Locate and identify every blood parasite.
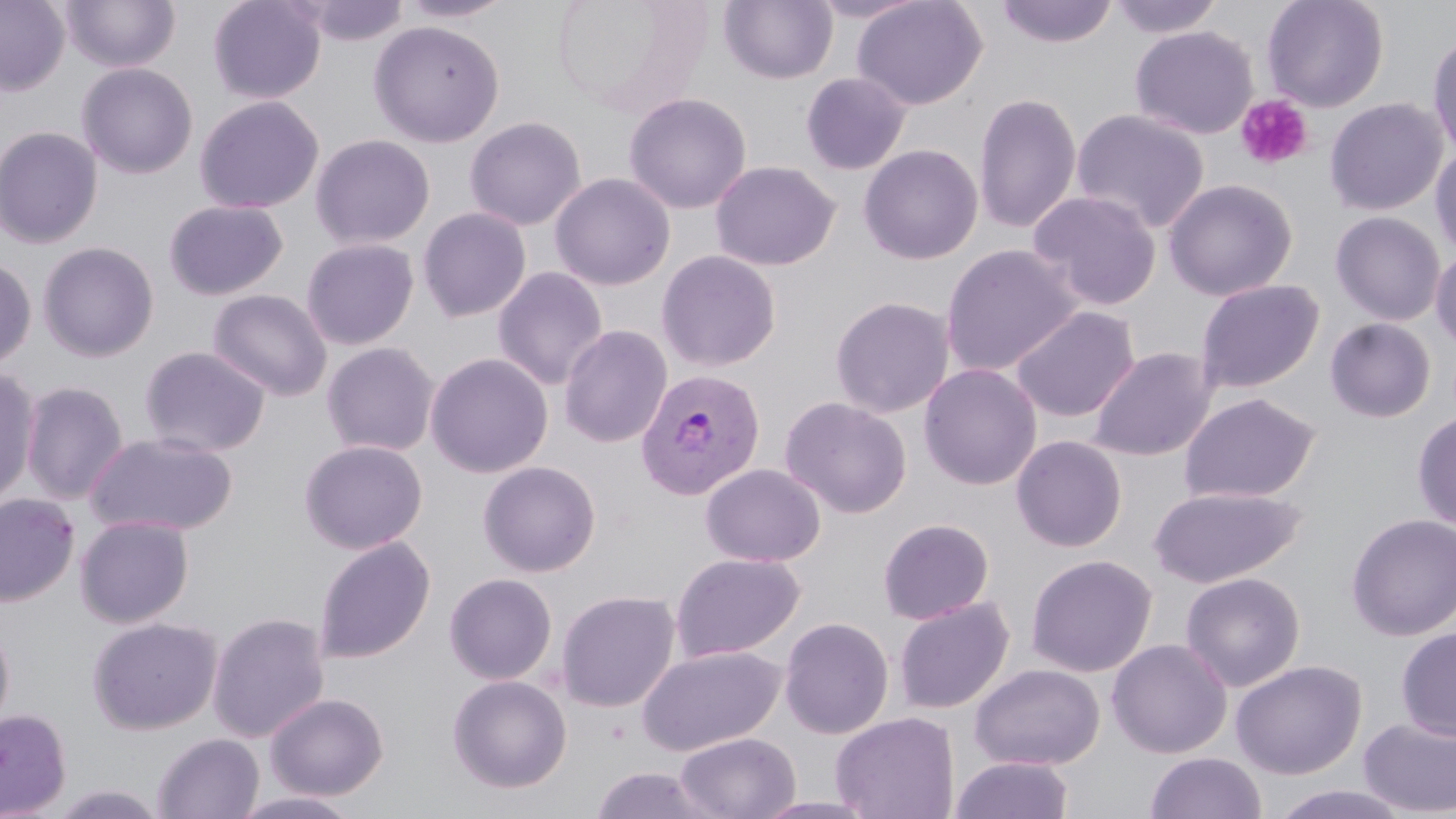

Approximate bounding boxes as named x1/y1/x2/y2 corners in pixels.
Plasmodium vivax-infected red blood cells: (x1=635, y1=368, x2=766, y2=501).
No Plasmodium falciparum, Plasmodium ovale, Plasmodium malariae, Babesia divergens, or Trypanosoma brucei observed.

Platelet locations: (x1=1236, y1=94, x2=1314, y2=170). Uninfected red blood cell locations: (x1=60, y1=0, x2=180, y2=72), (x1=208, y1=0, x2=326, y2=104), (x1=397, y1=0, x2=516, y2=23), (x1=551, y1=0, x2=709, y2=120), (x1=719, y1=0, x2=838, y2=84), (x1=808, y1=0, x2=928, y2=23), (x1=851, y1=0, x2=987, y2=110), (x1=995, y1=0, x2=1118, y2=48), (x1=1107, y1=0, x2=1225, y2=38), (x1=1262, y1=0, x2=1389, y2=112), (x1=0, y1=1, x2=70, y2=95), (x1=291, y1=1, x2=410, y2=46), (x1=369, y1=20, x2=505, y2=146), (x1=1130, y1=25, x2=1258, y2=139), (x1=1427, y1=31, x2=1456, y2=160), (x1=77, y1=62, x2=199, y2=179), (x1=800, y1=71, x2=911, y2=175), (x1=624, y1=92, x2=752, y2=214), (x1=973, y1=92, x2=1081, y2=234), (x1=194, y1=95, x2=324, y2=214), (x1=1324, y1=97, x2=1448, y2=216), (x1=1071, y1=108, x2=1211, y2=234), (x1=464, y1=116, x2=586, y2=231), (x1=0, y1=126, x2=104, y2=248), (x1=310, y1=134, x2=435, y2=250), (x1=858, y1=144, x2=983, y2=264), (x1=1429, y1=145, x2=1456, y2=257), (x1=710, y1=160, x2=840, y2=271), (x1=549, y1=172, x2=676, y2=291), (x1=1163, y1=178, x2=1298, y2=301), (x1=1027, y1=190, x2=1162, y2=310), (x1=163, y1=199, x2=289, y2=300), (x1=417, y1=206, x2=532, y2=323), (x1=1330, y1=211, x2=1446, y2=325), (x1=301, y1=238, x2=419, y2=350), (x1=37, y1=241, x2=159, y2=362), (x1=940, y1=243, x2=1082, y2=376), (x1=1430, y1=248, x2=1456, y2=352), (x1=656, y1=250, x2=781, y2=372), (x1=0, y1=257, x2=36, y2=371), (x1=492, y1=266, x2=608, y2=390), (x1=1195, y1=278, x2=1325, y2=394), (x1=207, y1=289, x2=332, y2=401), (x1=829, y1=296, x2=955, y2=418), (x1=1010, y1=306, x2=1140, y2=422), (x1=1325, y1=317, x2=1436, y2=422), (x1=559, y1=325, x2=672, y2=448), (x1=321, y1=342, x2=440, y2=457), (x1=139, y1=346, x2=270, y2=457), (x1=1088, y1=346, x2=1217, y2=461), (x1=425, y1=352, x2=553, y2=478), (x1=918, y1=363, x2=1042, y2=490), (x1=0, y1=368, x2=41, y2=507), (x1=20, y1=381, x2=129, y2=504), (x1=1179, y1=392, x2=1321, y2=504), (x1=779, y1=396, x2=912, y2=518), (x1=1413, y1=411, x2=1456, y2=532), (x1=85, y1=431, x2=239, y2=537), (x1=1011, y1=435, x2=1127, y2=552), (x1=299, y1=439, x2=428, y2=554), (x1=478, y1=460, x2=601, y2=578), (x1=700, y1=463, x2=826, y2=567), (x1=1147, y1=486, x2=1305, y2=588), (x1=0, y1=493, x2=80, y2=607), (x1=1346, y1=513, x2=1456, y2=640), (x1=74, y1=515, x2=194, y2=628), (x1=878, y1=518, x2=994, y2=625), (x1=313, y1=537, x2=436, y2=664), (x1=670, y1=552, x2=805, y2=662), (x1=1025, y1=554, x2=1157, y2=677), (x1=1180, y1=571, x2=1305, y2=692), (x1=444, y1=573, x2=558, y2=685), (x1=555, y1=589, x2=680, y2=712), (x1=893, y1=596, x2=1015, y2=714), (x1=207, y1=612, x2=330, y2=743), (x1=778, y1=616, x2=894, y2=739), (x1=88, y1=617, x2=222, y2=735), (x1=0, y1=619, x2=15, y2=739), (x1=1395, y1=626, x2=1456, y2=740), (x1=1106, y1=638, x2=1232, y2=759), (x1=637, y1=644, x2=786, y2=756), (x1=1230, y1=659, x2=1367, y2=779), (x1=969, y1=663, x2=1105, y2=770), (x1=447, y1=674, x2=572, y2=793), (x1=265, y1=692, x2=389, y2=801), (x1=0, y1=709, x2=72, y2=818), (x1=830, y1=712, x2=959, y2=819), (x1=1359, y1=716, x2=1456, y2=817), (x1=674, y1=732, x2=801, y2=818), (x1=152, y1=733, x2=264, y2=818), (x1=1145, y1=751, x2=1267, y2=819), (x1=951, y1=756, x2=1073, y2=818), (x1=590, y1=765, x2=717, y2=819), (x1=50, y1=784, x2=167, y2=819), (x1=1269, y1=785, x2=1414, y2=819), (x1=230, y1=790, x2=365, y2=818), (x1=751, y1=795, x2=880, y2=818). Slide-level diagnosis: Plasmodium vivax. Light microscopy. May-Grünwald-Giemsa-stained preparation. Thin blood film. One field of a larger specimen. Image is 1456×819 pixels. 1000x magnification.